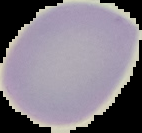
Image is 142×133 pixels. Malaria status: uninfected. The area outside the segmented cell region is set to black. From a thin blood smear.